Point out malaria parasites and leukocytes.
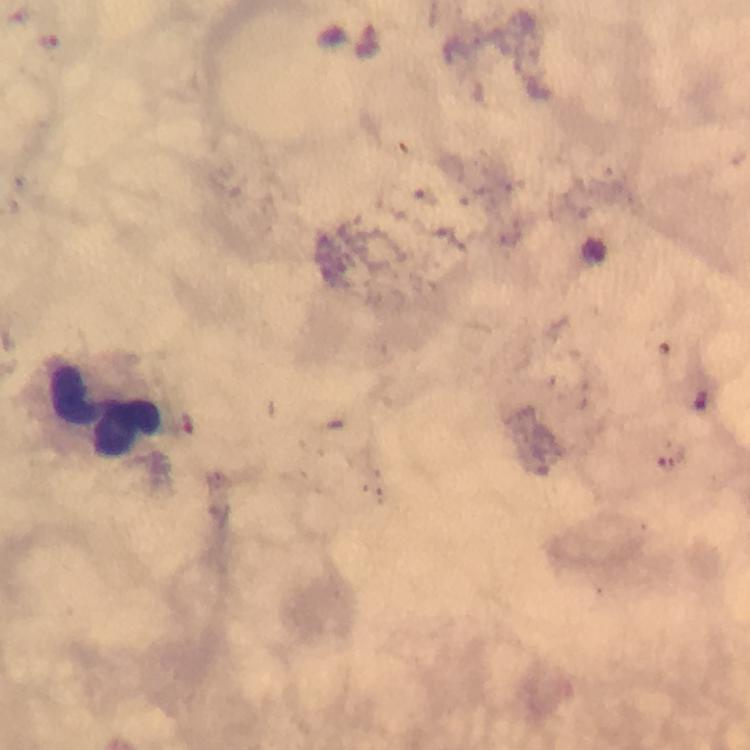
No malaria parasites seen.
Approximate centers as (x, y) in pixels.
Leukocytes: (113, 409).

100x magnification. Immersion oil was used. Giemsa stain. Thick smear. Image is 750×750 pixels. Photographed with a smartphone mounted on the microscope. A crop from one field of view. From a diagnostic examination for malaria.